Classify this cell by malaria status.
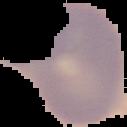

It is uninfected.

image type = cell region segmented out of the field of view; surrounding area masked to black
image size = 127×127 pixels
preparation = thin blood film